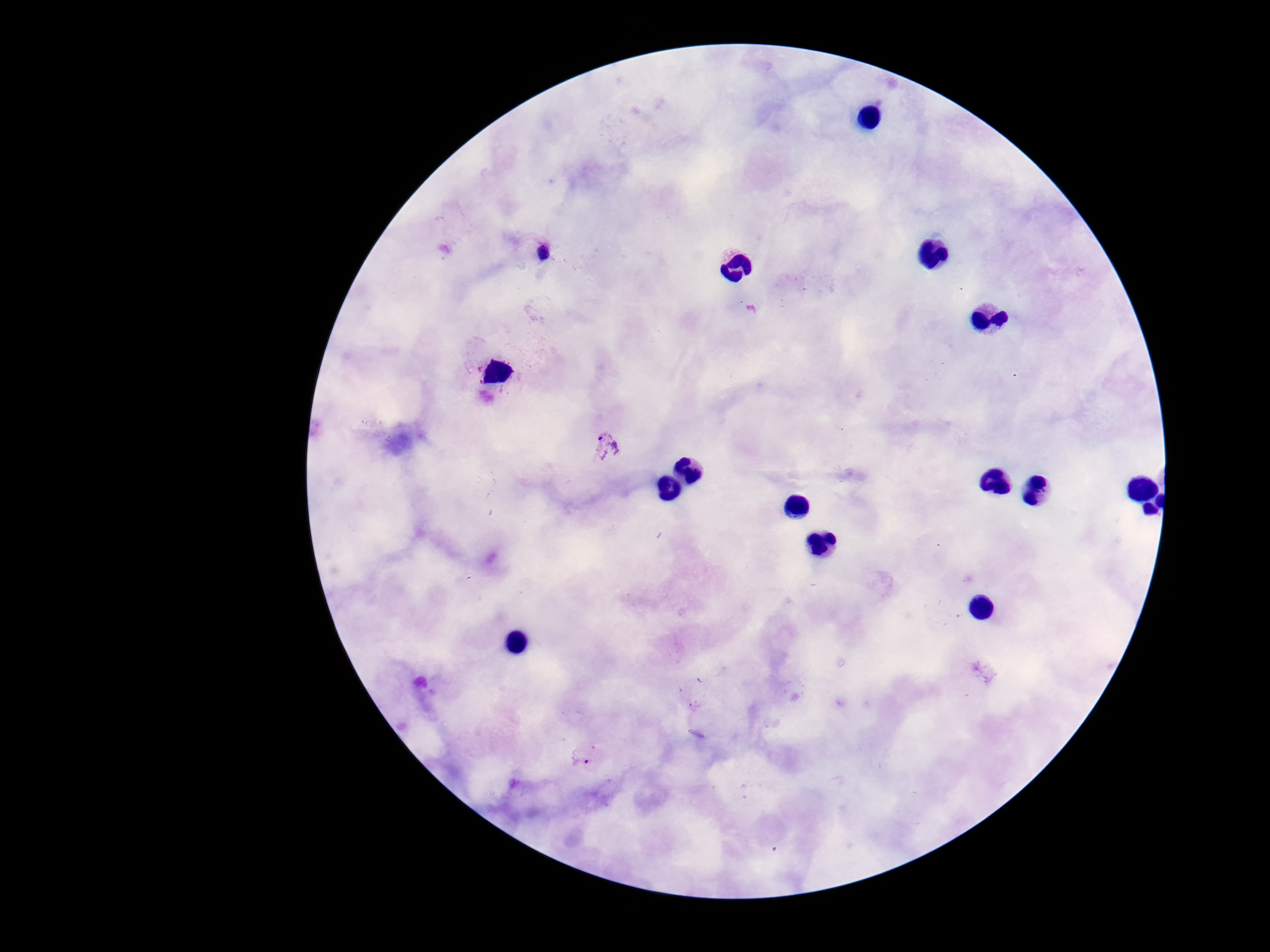

Approximate centers as (x, y) in pixels.
Summary:
  - Plasmodium parasite locations: (536, 250), (607, 448), (590, 756)
  - Magnification: 100x
  - Image size: 1270×952 pixels
  - Stain: Giemsa
  - Patient malaria status: positive
  - Preparation: thick peripheral-blood smear
  - Field of view: single
  - Capture: smartphone camera through the microscope eyepiece